Give the position of every malaria parasite.
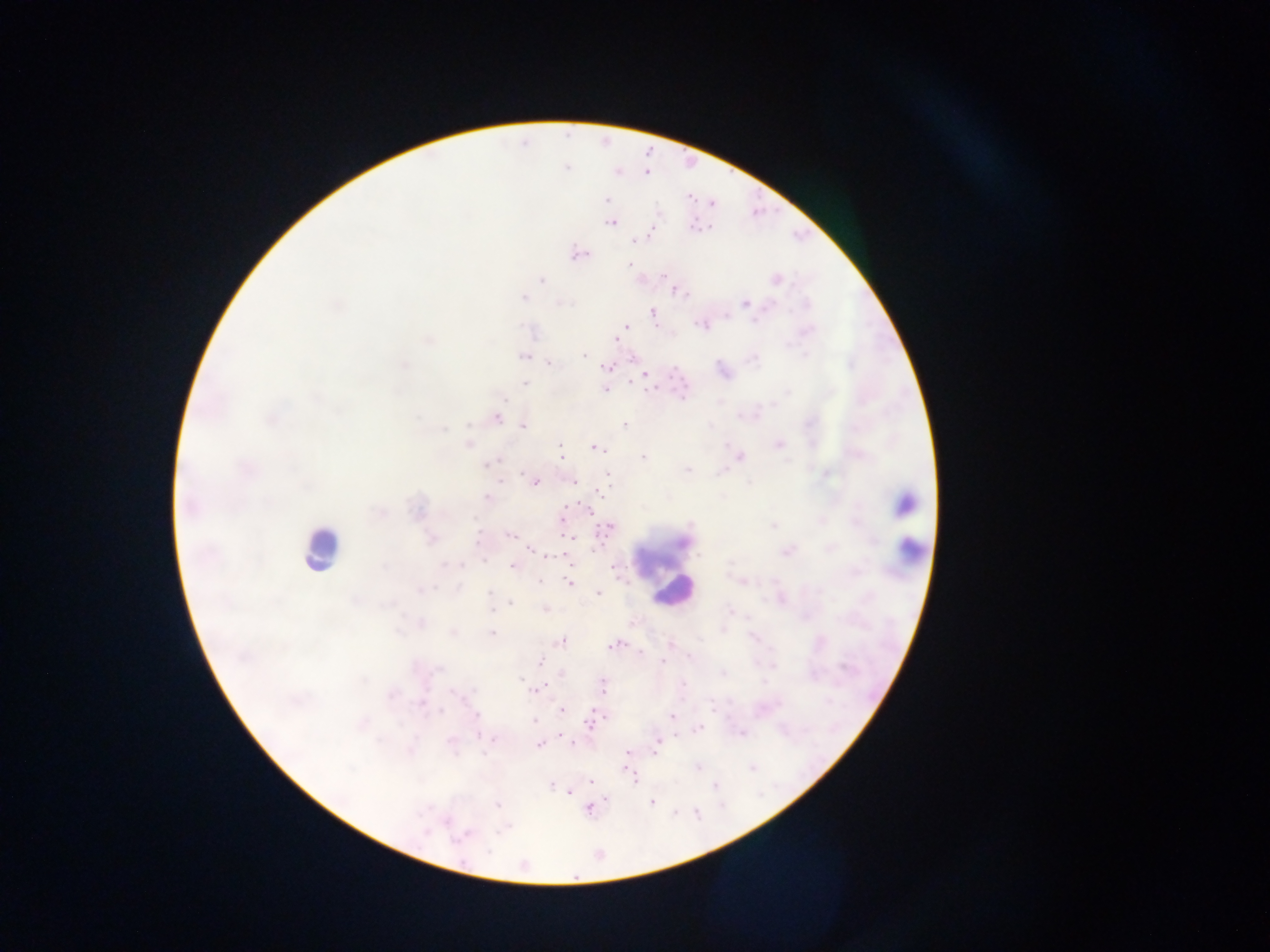

Approximate centers as (x, y) in pixels.
Malaria parasites: (646, 171), (606, 201), (611, 222), (650, 229), (632, 240), (578, 254), (630, 264), (666, 273), (775, 279), (542, 280), (674, 289), (523, 298), (559, 302), (745, 304), (653, 312), (702, 323), (624, 327), (619, 334), (616, 339), (584, 354), (523, 356), (548, 361), (607, 367), (645, 375), (525, 384), (605, 389), (497, 417), (624, 424), (523, 425), (469, 443), (779, 445), (597, 448), (561, 454), (739, 455), (643, 457), (488, 462), (686, 470), (606, 474), (572, 480), (534, 481), (600, 491), (487, 498), (590, 509), (820, 519), (772, 526), (606, 528), (510, 535), (569, 535), (431, 539), (830, 548), (531, 549), (788, 551), (565, 554), (512, 566), (612, 566), (742, 581), (567, 583), (599, 592), (511, 603), (544, 608), (419, 623), (723, 628), (453, 631), (492, 631), (562, 640), (618, 644), (670, 644), (662, 661), (540, 663), (603, 686), (536, 689), (423, 704), (560, 711), (476, 716), (604, 716), (672, 716), (535, 720), (591, 722), (698, 728), (741, 733), (493, 738), (450, 741), (573, 742), (538, 743), (657, 743), (628, 752), (630, 774), (590, 781), (551, 785), (568, 790), (652, 802), (496, 804), (588, 806).

image_size: 1270×952 pixels
field_of_view: single
capture: mobile-phone photograph through a microscope
preparation: thick blood film
leukocyte_locations: 'approximate centers as (x, y) in pixels: (906, 504), (320, 547), (911, 552), (663, 564), (674, 591)'
country: Ghana